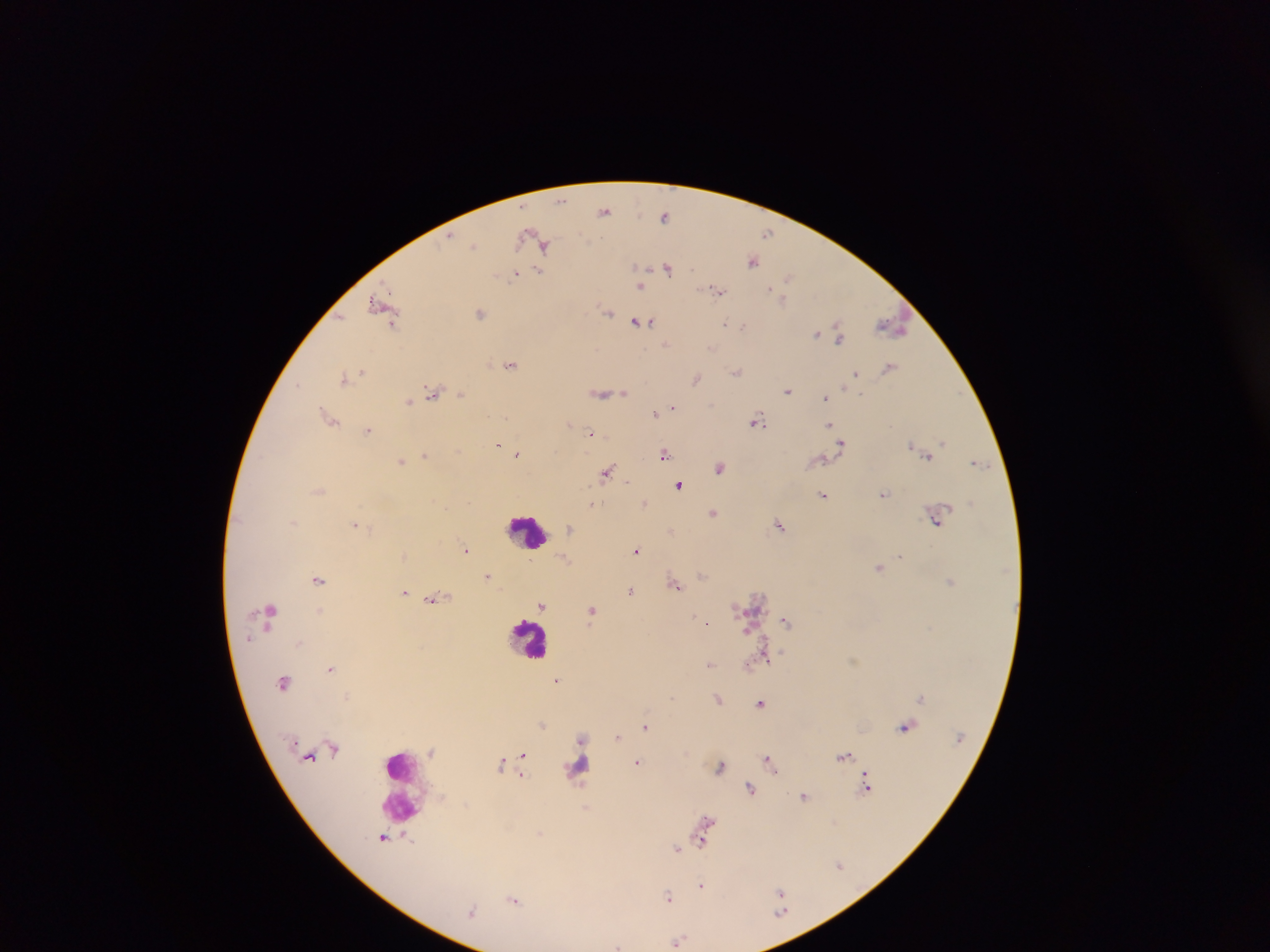
Approximate centers as [x, y] in pixels.
Summary:
  - Plasmodium parasite locations: [562, 201], [604, 210], [664, 216], [768, 233], [525, 237], [474, 245], [545, 246], [752, 261], [635, 266], [668, 267], [539, 271], [516, 274], [788, 278], [642, 286], [771, 288], [716, 291], [783, 300], [381, 305], [608, 311], [480, 313], [641, 323], [725, 323], [392, 324], [892, 324], [743, 327], [817, 333], [839, 336], [667, 344], [710, 348], [511, 365], [888, 367], [362, 371], [736, 371], [856, 373], [344, 378], [696, 379], [298, 384], [788, 391], [433, 392], [460, 393], [602, 393], [624, 393], [825, 397], [408, 401], [674, 407], [654, 413], [330, 418], [756, 422], [570, 423], [829, 425], [367, 430], [590, 432], [943, 442], [841, 443], [498, 445], [911, 445], [517, 454], [663, 454], [424, 455], [927, 458], [402, 462], [977, 462], [720, 467], [607, 472], [627, 482], [679, 485], [884, 494], [823, 495], [645, 502], [592, 503], [713, 513], [937, 520], [355, 524], [779, 525], [569, 527], [672, 530], [466, 549], [636, 550], [901, 556], [879, 567], [702, 574], [488, 575], [318, 579], [950, 582], [675, 585], [630, 591], [404, 592], [435, 599], [541, 605], [592, 611], [271, 612], [786, 621], [707, 622], [248, 638], [300, 643], [767, 657], [710, 664], [749, 665], [331, 668], [557, 680], [284, 683], [921, 697], [718, 699], [760, 703], [542, 725], [645, 727], [905, 727], [581, 737], [617, 737], [523, 754], [844, 756], [769, 760], [637, 762], [501, 763], [721, 766], [772, 766], [866, 784], [750, 788], [804, 797], [707, 820], [384, 838], [408, 839], [703, 841], [677, 848], [839, 865], [702, 885], [781, 892], [667, 896], [514, 900], [472, 912], [678, 940], [617, 945]
  - Leukocyte locations: [525, 531], [531, 638], [401, 773]
  - Country: Ghana
  - Image size: 1270×952 pixels
  - Preparation: thick blood film
  - Field of view: single
  - Capture: mobile-phone photograph through a microscope